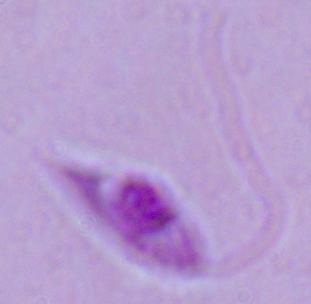

A Leishmania parasite is shown. 1000x magnification. Photomicrograph.